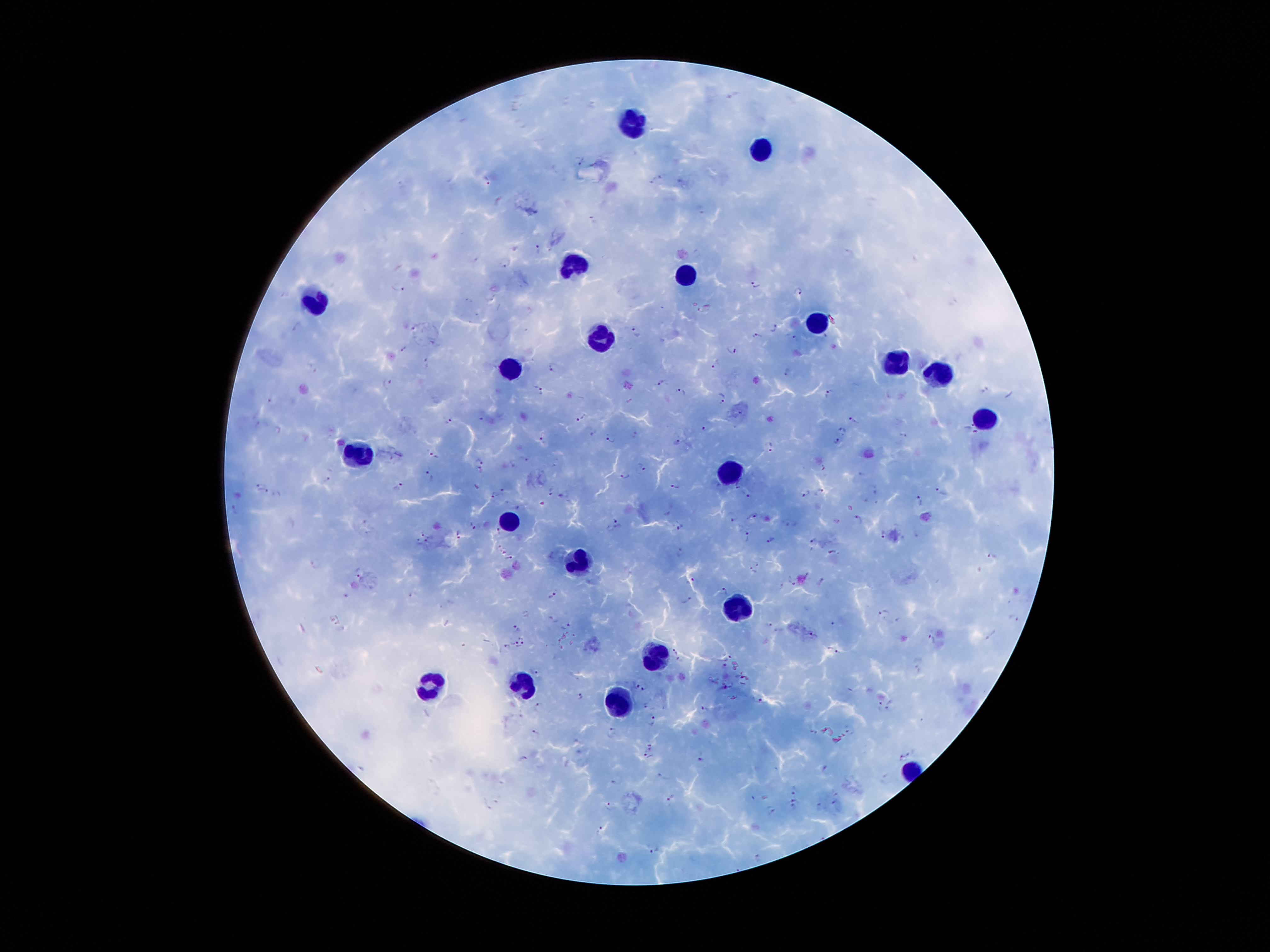
coordinate format = approximate centers as (x, y) in pixels
Plasmodium parasite locations = (579, 159), (663, 175), (487, 179), (653, 182), (701, 209), (592, 220), (537, 247), (504, 262), (755, 283), (400, 287), (799, 291), (470, 300), (528, 311), (295, 326), (416, 326), (775, 328), (636, 331), (757, 336), (790, 336), (435, 342), (403, 348), (731, 349), (428, 362), (716, 364), (553, 366), (787, 371), (386, 381), (660, 384), (538, 390), (680, 392), (829, 394), (721, 398), (580, 418), (448, 419), (855, 420), (704, 429), (593, 431), (971, 431), (634, 432), (843, 432), (904, 433), (543, 437), (610, 438), (675, 441), (838, 442), (771, 446), (433, 455), (523, 459), (480, 461), (513, 461), (641, 466), (824, 467), (478, 472), (625, 474), (860, 474), (430, 475), (327, 478), (258, 484), (399, 486), (674, 486), (477, 487), (264, 491), (502, 491), (550, 491), (820, 491), (747, 493), (806, 493), (941, 493), (495, 494), (562, 495), (920, 500), (233, 511), (753, 515), (859, 519), (734, 520), (617, 523), (473, 525), (680, 528), (499, 531), (884, 532), (424, 534), (460, 535), (749, 536), (771, 539), (815, 541), (418, 542), (428, 543), (503, 550), (832, 551), (680, 552), (993, 558), (510, 559), (757, 563), (752, 569), (358, 573), (821, 580), (691, 581), (793, 582), (724, 591), (412, 594), (553, 594), (687, 599), (886, 614), (1013, 618), (834, 620), (565, 624), (769, 624), (516, 627), (813, 635), (994, 636), (931, 638), (514, 641), (522, 645), (507, 646), (675, 651), (835, 651), (730, 656), (681, 662), (725, 665), (535, 670), (640, 686), (725, 686), (580, 697), (759, 699), (891, 704), (540, 706), (880, 706), (705, 709), (650, 719), (849, 729), (612, 730), (535, 731), (652, 746), (914, 752), (702, 754), (646, 757), (523, 758), (899, 759), (825, 769), (663, 777), (887, 778), (617, 779), (794, 791), (836, 791), (671, 797), (790, 798), (835, 805), (610, 806), (793, 807), (771, 809), (599, 832), (652, 847), (759, 858)
leukocyte locations = (639, 120), (764, 150), (577, 264), (685, 276), (319, 301), (814, 322), (603, 338), (891, 361), (508, 372), (937, 374), (987, 416), (364, 460), (729, 472), (511, 516), (581, 565), (740, 607), (659, 657), (522, 681), (431, 687), (620, 701)
image size = 1270×952 pixels
preparation = thick peripheral-blood smear
field of view = single
patient malaria status = infected with Plasmodium falciparum
stain = Giemsa
magnification = 100x
capture = smartphone camera through the microscope eyepiece